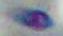
Micrograph. 1000x magnification. Toxoplasma gondii is seen.